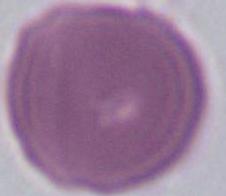

Summary:
  - Identification: erythrocyte
  - Modality: micrograph
  - Magnification: 1000x